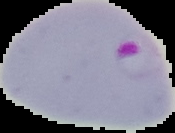
{
  "image_type": "segmented cell region on a black background",
  "image_size": "175×133 pixels",
  "result": "Plasmodium parasites identified",
  "preparation": "thin blood film"
}